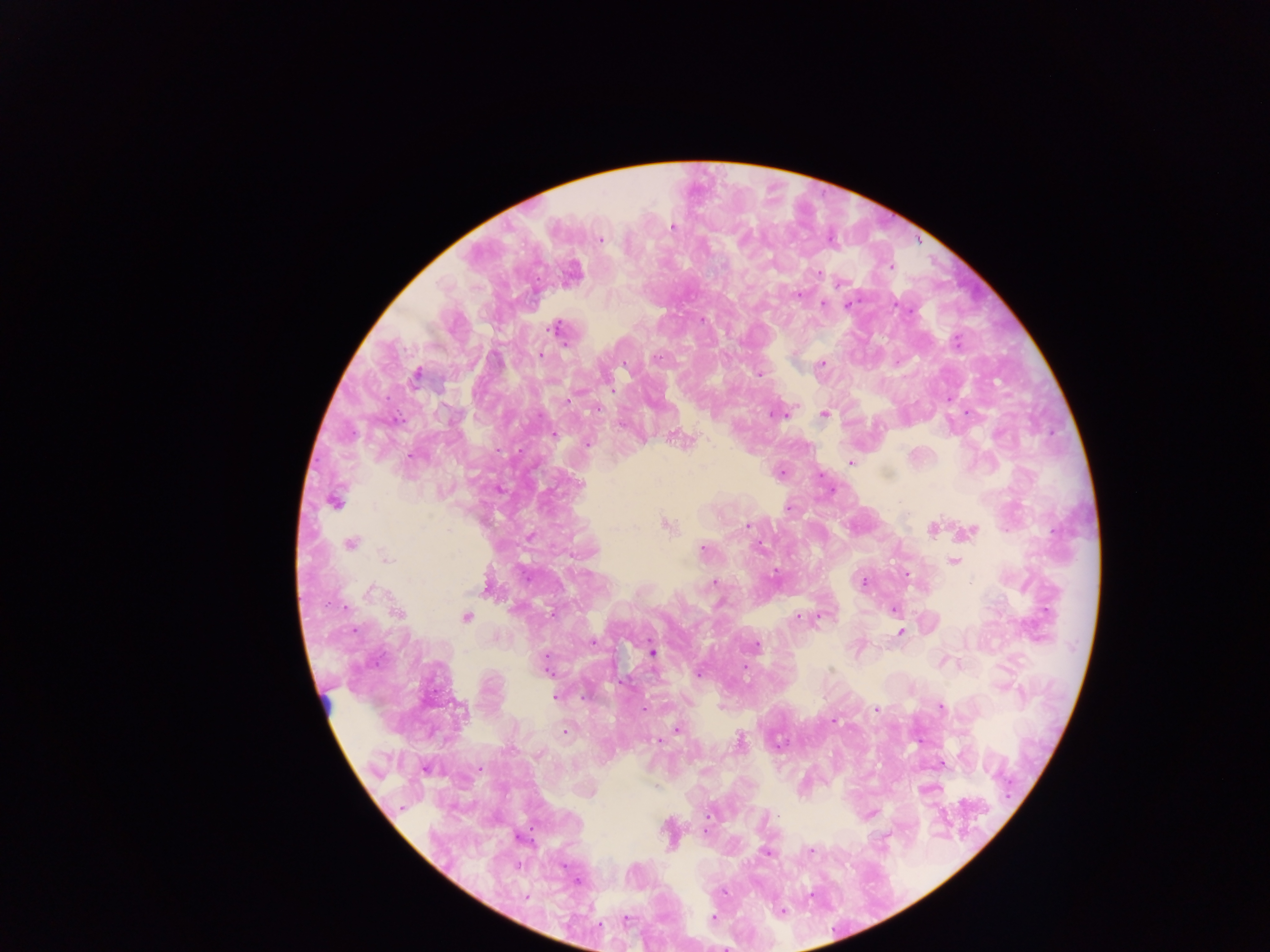

{
  "preparation": "thick blood film",
  "image_size": "1270×952 pixels",
  "capture": "mobile-phone photograph through a microscope",
  "field_of_view": "single",
  "leukocyte_locations": "approximate centers as (x, y) in pixels: (326, 709)",
  "country": "Ghana",
  "malaria_parasite_locations": "approximate centers as (x, y) in pixels: (672, 227), (742, 238), (600, 239), (889, 267), (819, 273), (840, 283), (798, 294), (823, 304), (847, 304), (895, 304), (701, 320), (557, 328), (956, 342), (540, 355), (657, 358), (821, 364), (416, 374), (759, 374), (569, 401), (598, 409), (776, 414), (824, 414), (554, 435), (588, 444), (851, 462), (781, 473), (579, 484), (335, 501), (789, 508), (666, 524), (748, 525), (932, 529), (970, 531), (351, 543), (759, 547), (703, 549), (386, 559), (954, 562), (774, 572), (864, 581), (714, 583), (484, 588), (372, 592), (892, 609), (398, 613), (551, 614), (466, 617), (797, 618), (900, 633), (592, 642), (756, 644), (652, 652), (546, 666), (745, 668), (699, 674), (555, 698), (584, 698), (940, 707), (876, 709), (833, 721), (678, 730), (565, 731), (659, 741), (740, 741), (779, 744), (426, 769), (479, 769), (871, 814), (777, 815), (705, 831), (811, 851), (765, 852), (577, 881), (810, 895), (526, 897), (782, 911), (713, 918), (626, 920)"
}